Assess the morphology of the erythrocytes.
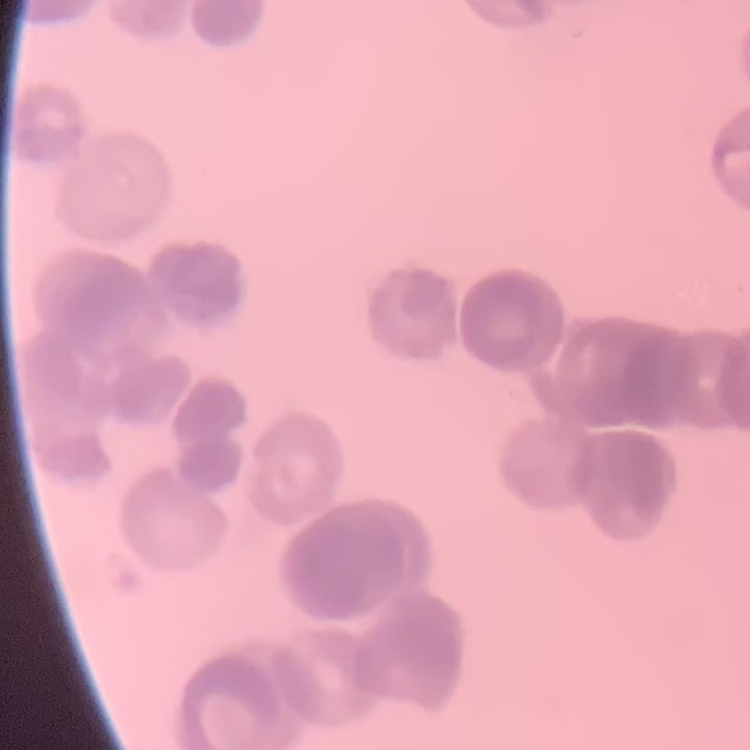
They show rouleaux formation.

stain: Field's or Giemsa
image_type: one tile cut from a larger photomicrograph
preparation: thin peripheral smear